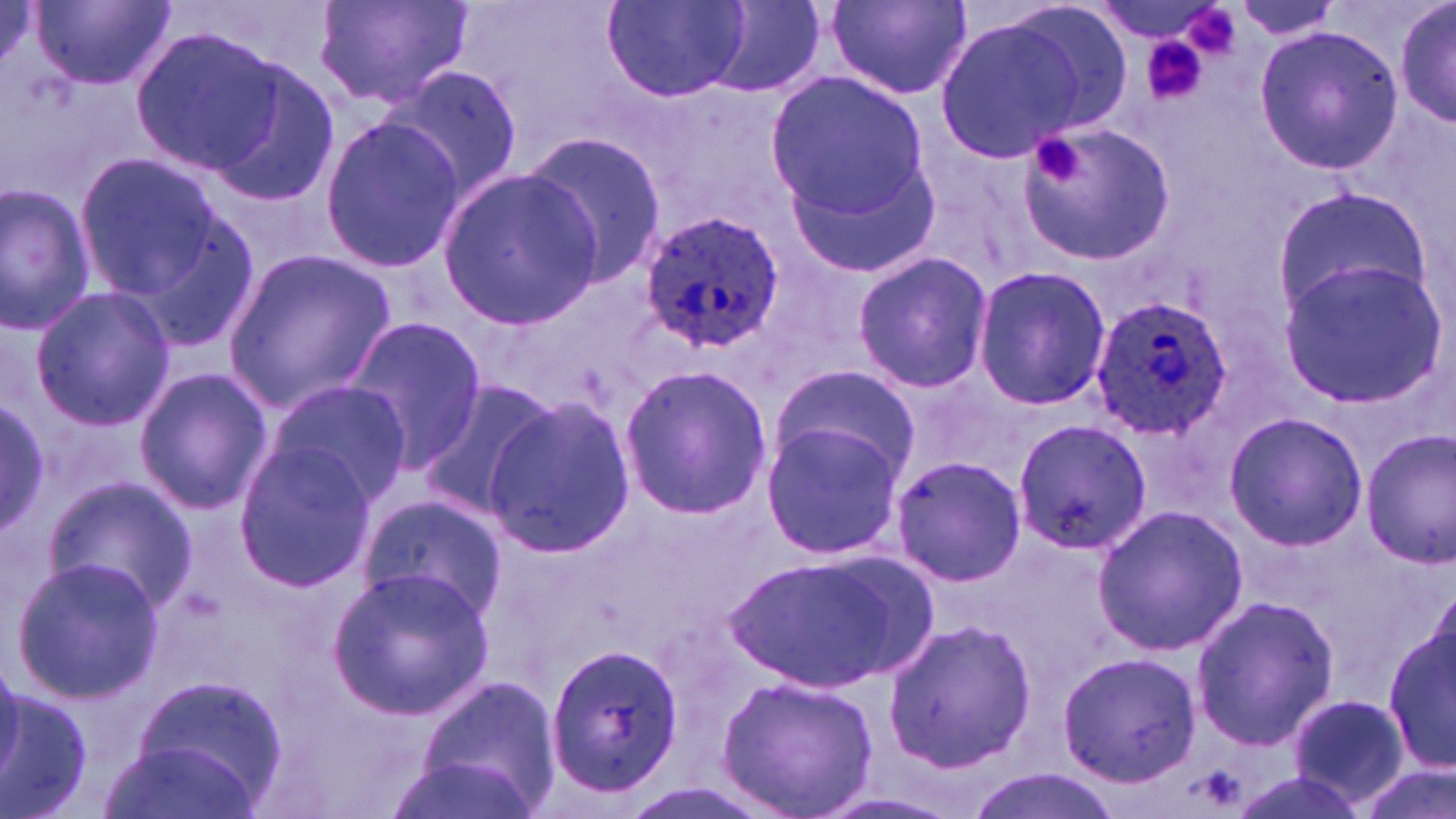
Summary:
  - Coordinate format: approximate bounding boxes as named x1/y1/x2/y2 corners in pixels
  - Uninfected red blood cell locations: (x1=31, y1=0, x2=175, y2=88), (x1=315, y1=0, x2=471, y2=111), (x1=603, y1=0, x2=751, y2=101), (x1=702, y1=0, x2=826, y2=98), (x1=826, y1=0, x2=973, y2=98), (x1=1391, y1=0, x2=1454, y2=132), (x1=1232, y1=1, x2=1342, y2=41), (x1=1089, y1=2, x2=1228, y2=45), (x1=931, y1=8, x2=1115, y2=162), (x1=1254, y1=26, x2=1401, y2=174), (x1=129, y1=28, x2=282, y2=176), (x1=199, y1=52, x2=342, y2=210), (x1=385, y1=66, x2=524, y2=207), (x1=766, y1=67, x2=928, y2=222), (x1=319, y1=113, x2=468, y2=276), (x1=1021, y1=120, x2=1175, y2=265), (x1=519, y1=129, x2=667, y2=287), (x1=75, y1=153, x2=225, y2=301), (x1=788, y1=153, x2=939, y2=277), (x1=438, y1=168, x2=601, y2=326), (x1=0, y1=181, x2=96, y2=334), (x1=1275, y1=186, x2=1430, y2=314), (x1=128, y1=209, x2=263, y2=356), (x1=222, y1=248, x2=395, y2=414), (x1=850, y1=251, x2=993, y2=395), (x1=1278, y1=258, x2=1444, y2=406), (x1=971, y1=265, x2=1111, y2=412), (x1=27, y1=285, x2=176, y2=430), (x1=340, y1=317, x2=485, y2=475), (x1=767, y1=362, x2=919, y2=489), (x1=618, y1=365, x2=774, y2=518), (x1=133, y1=369, x2=271, y2=514), (x1=263, y1=377, x2=410, y2=505), (x1=414, y1=378, x2=561, y2=519), (x1=480, y1=396, x2=637, y2=555), (x1=0, y1=400, x2=52, y2=534), (x1=1223, y1=412, x2=1368, y2=550), (x1=758, y1=419, x2=908, y2=564), (x1=1013, y1=419, x2=1150, y2=556), (x1=1361, y1=430, x2=1456, y2=568), (x1=231, y1=441, x2=379, y2=587), (x1=890, y1=455, x2=1027, y2=587), (x1=46, y1=475, x2=196, y2=611), (x1=356, y1=495, x2=507, y2=622), (x1=1093, y1=504, x2=1249, y2=658), (x1=721, y1=552, x2=924, y2=691), (x1=10, y1=555, x2=162, y2=704), (x1=327, y1=566, x2=493, y2=718), (x1=1189, y1=595, x2=1340, y2=749), (x1=1387, y1=603, x2=1454, y2=782), (x1=883, y1=619, x2=1038, y2=770), (x1=544, y1=639, x2=685, y2=797), (x1=1056, y1=650, x2=1202, y2=789), (x1=716, y1=673, x2=878, y2=818), (x1=415, y1=676, x2=560, y2=812), (x1=0, y1=685, x2=94, y2=819), (x1=124, y1=686, x2=282, y2=813), (x1=1286, y1=694, x2=1408, y2=808), (x1=101, y1=737, x2=259, y2=819), (x1=385, y1=752, x2=538, y2=819), (x1=1356, y1=760, x2=1454, y2=819), (x1=960, y1=768, x2=1127, y2=819)
  - Platelet locations: (x1=1136, y1=32, x2=1215, y2=106), (x1=1031, y1=132, x2=1090, y2=188)
  - Plasmodium ovale-infected red blood cell locations: (x1=638, y1=209, x2=787, y2=356), (x1=1088, y1=296, x2=1231, y2=441)
  - Slide-level diagnosis: Plasmodium ovale
  - Magnification: 1000x
  - Modality: optical microscopy
  - Field of view: one of a larger specimen
  - Stain: May-Grünwald-Giemsa
  - Image size: 1456×819 pixels
  - Preparation: thin blood smear